Identify the parasite.
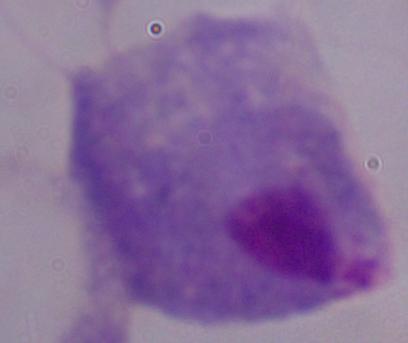
A trichomonad.

modality = micrograph
magnification = 1000x